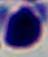 A white blood cell is shown. 1000x magnification. Micrograph.